Report the malaria status of this cell.
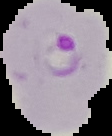
Parasitized.

preparation = thin blood film
image type = cell region segmented out of the field of view; surrounding area masked to black
image size = 112×136 pixels